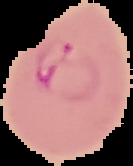

preparation = thin blood smear
result = Plasmodium parasites detected
image type = segmented cell region with the area outside set to black
image size = 133×166 pixels